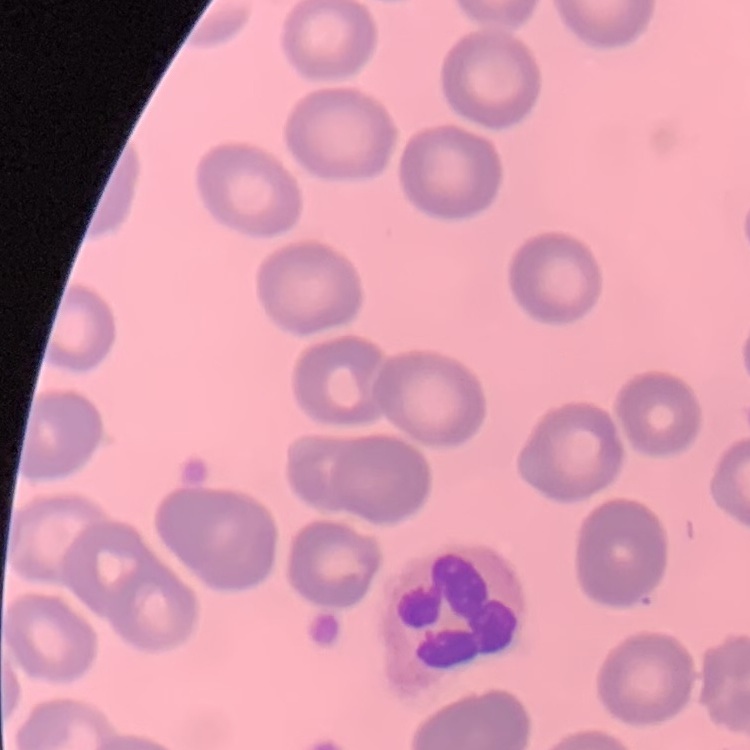

The red blood cells exhibit no rouleaux formation. Thin peripheral smear. One tile cut from a larger photomicrograph. Stained with either Field's or Giemsa.